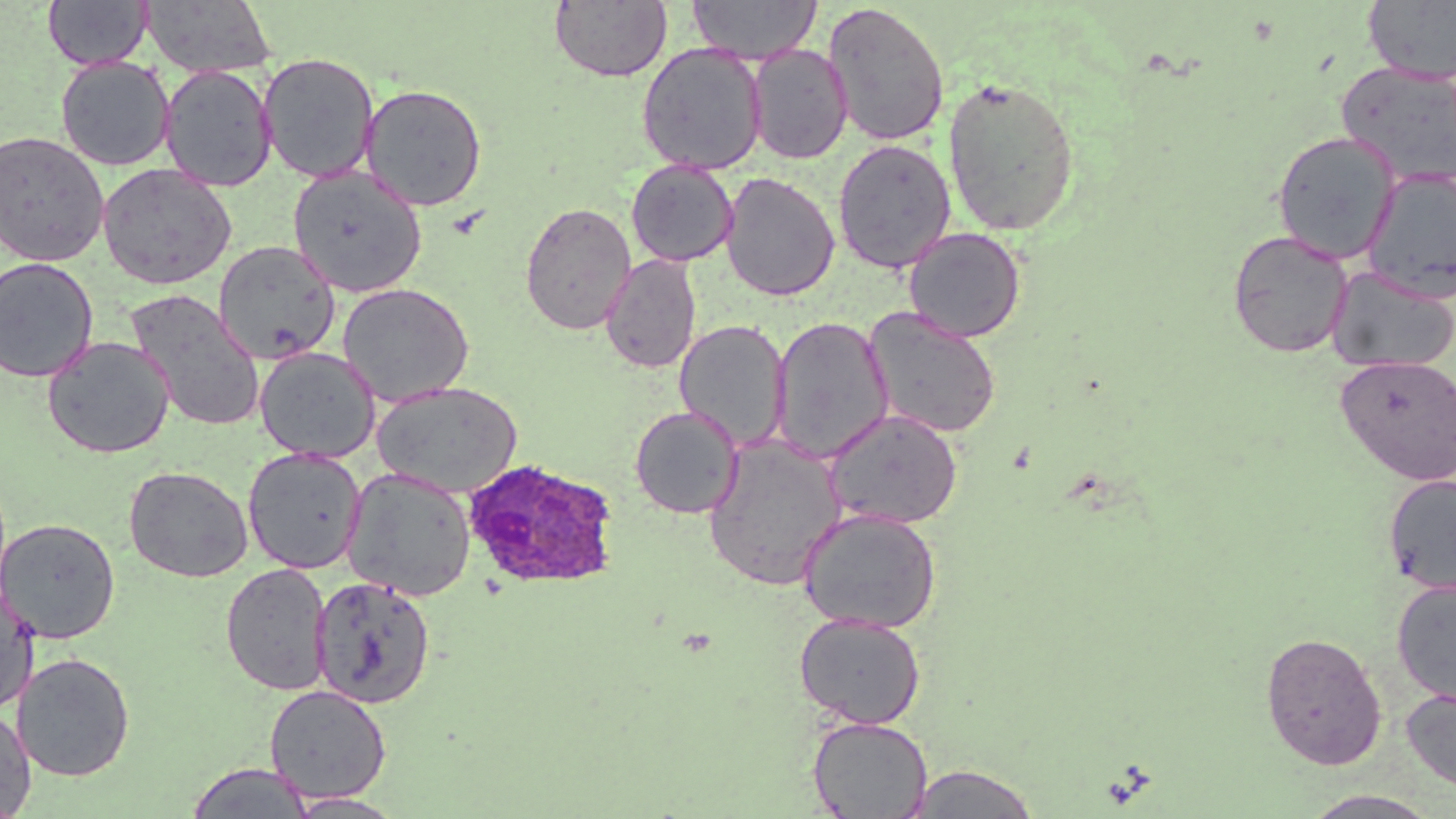

Summary:
  - Coordinate format: approximate bounding boxes as (x1,y1)-(x2,y2) corner pairs in pixels
  - Uninfected red blood cell locations: (43,0)-(152,70), (549,0)-(672,83), (687,0)-(821,64), (140,1)-(276,78), (1362,1)-(1456,84), (822,2)-(950,147), (636,43)-(767,175), (747,44)-(852,164), (258,53)-(380,183), (55,56)-(175,171), (1337,61)-(1456,188), (159,65)-(277,192), (942,76)-(1081,236), (360,83)-(488,212), (1272,130)-(1401,264), (0,131)-(109,267), (832,138)-(956,274), (626,160)-(738,267), (97,163)-(236,290), (288,166)-(426,298), (1362,167)-(1456,303), (720,171)-(839,302), (519,201)-(636,335), (904,226)-(1026,342), (1227,229)-(1354,358), (213,240)-(340,365), (601,254)-(701,373), (0,256)-(99,383), (1326,266)-(1456,374), (337,282)-(474,407), (127,290)-(266,432), (864,307)-(1002,438), (770,316)-(893,465), (674,319)-(791,452), (42,336)-(174,458), (254,346)-(380,462), (1335,355)-(1456,485), (372,381)-(523,497), (629,405)-(743,519), (824,408)-(962,529), (703,434)-(846,591), (243,447)-(366,573), (124,465)-(253,582), (342,467)-(477,601), (1383,473)-(1456,596), (798,508)-(941,633), (0,517)-(120,643), (221,562)-(332,696), (311,575)-(436,709), (1391,578)-(1456,707), (0,585)-(39,716), (793,611)-(926,728), (1260,631)-(1386,770), (12,652)-(136,782), (264,684)-(392,803), (1401,686)-(1456,795), (0,707)-(37,818), (807,716)-(932,819), (185,762)-(315,818), (905,763)-(1041,818), (1298,789)-(1446,818), (286,792)-(405,818)
  - Plasmodium ovale-infected red blood cell locations: (462,457)-(620,590)
  - Slide-level diagnosis: Plasmodium ovale
  - Image size: 1456×819 pixels
  - Preparation: thin blood film
  - Stain: May-Grünwald-Giemsa
  - Magnification: 1000x
  - Field of view: one of a larger specimen
  - Modality: light microscopy